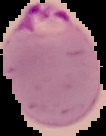

Segmented cell region on a black background. Image is 106×136 pixels. From a thin blood film. Malaria status: parasitized.